Locate every uninfected red blood cell.
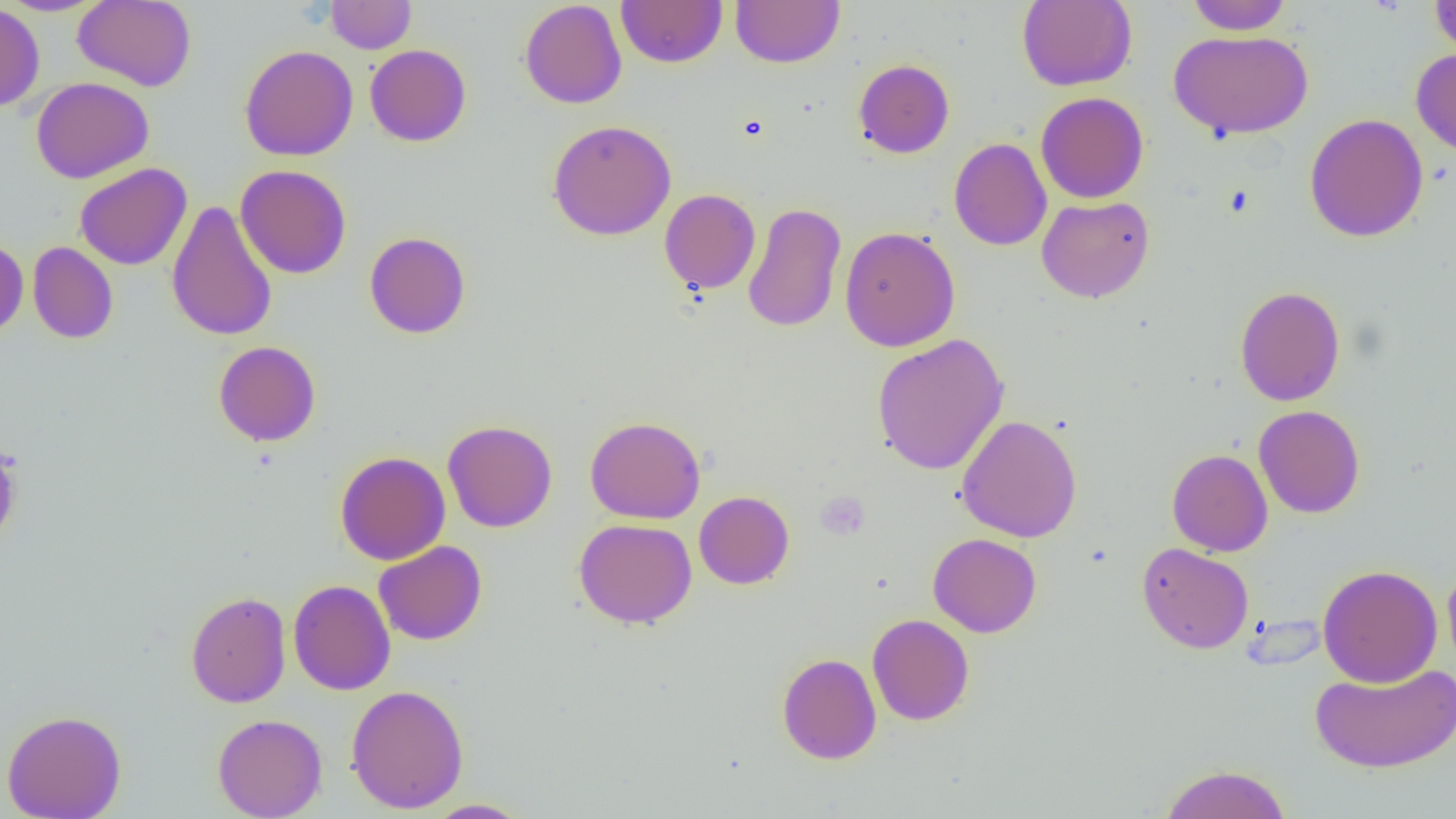

Approximate bounding boxes as [x1, y1, x2, y2] in pixels.
Uninfected red blood cells: [1, 0, 109, 16], [73, 0, 196, 91], [325, 0, 416, 54], [519, 0, 627, 109], [616, 0, 728, 67], [730, 0, 845, 68], [1017, 0, 1137, 91], [1184, 0, 1294, 34], [1430, 0, 1456, 57], [0, 3, 45, 112], [1168, 30, 1313, 141], [239, 44, 358, 161], [365, 44, 471, 147], [1410, 47, 1456, 157], [853, 58, 955, 159], [31, 77, 154, 183], [1035, 92, 1149, 203], [1304, 113, 1429, 242], [547, 119, 677, 241], [949, 138, 1052, 251], [75, 163, 191, 270], [235, 164, 351, 279], [659, 188, 760, 294], [1037, 196, 1154, 303], [166, 200, 278, 342], [742, 202, 846, 333], [839, 226, 960, 352], [364, 231, 471, 339], [0, 238, 28, 338], [27, 242, 118, 344], [1234, 285, 1346, 406], [871, 333, 1010, 475], [213, 341, 321, 447], [1253, 405, 1365, 518], [955, 414, 1082, 542], [585, 416, 705, 524], [443, 419, 557, 533], [0, 440, 22, 548], [1167, 448, 1273, 556], [335, 451, 451, 565], [694, 491, 794, 590], [574, 518, 697, 629], [928, 533, 1042, 638], [373, 541, 487, 645], [1137, 542, 1254, 654], [1442, 564, 1456, 677], [1317, 565, 1443, 687], [288, 579, 395, 696], [185, 590, 291, 708], [867, 613, 975, 726], [777, 652, 882, 765], [1310, 662, 1455, 773], [345, 684, 469, 814], [1, 709, 127, 819], [212, 713, 327, 819], [1157, 763, 1292, 819], [422, 799, 533, 818].

slide-level diagnosis = no evidence of blood parasites
preparation = thin blood film
magnification = 1000x
field of view = one of a larger specimen
image size = 1456×819 pixels
platelet locations = approximate bounding boxes as [x1, y1, x2, y2] in pixels: [815, 491, 870, 540]
modality = optical microscopy